State the preparation type.
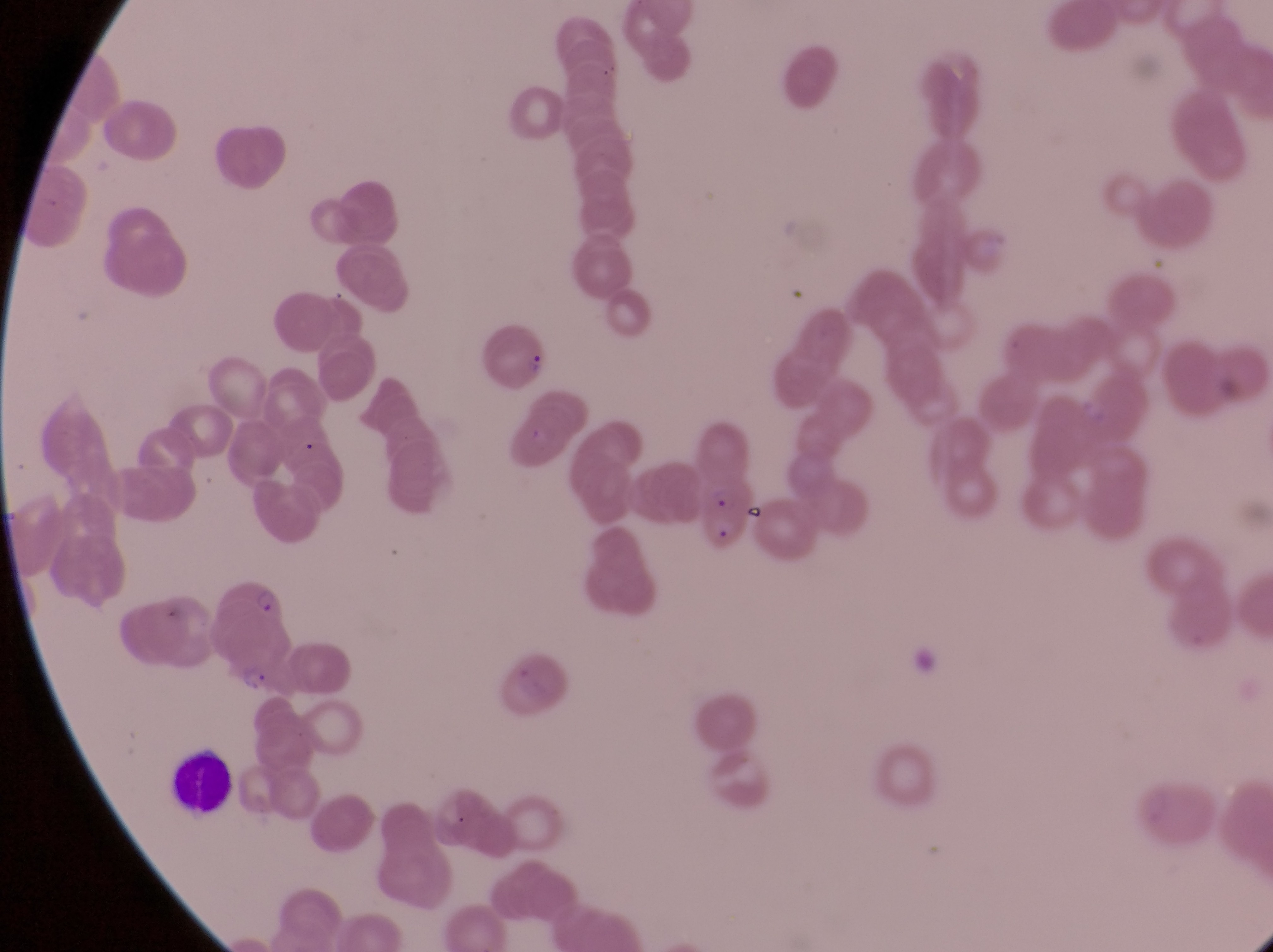

Thin blood smear.

Approximate bounding boxes as (left, top, right, bottom) in pixels.
Summary:
  - Leukocyte locations: (167, 754, 237, 816)
  - Parasitised red blood cell locations: (691, 475, 760, 552)
  - Trophozoite locations: (248, 580, 290, 619), (235, 661, 272, 698)
  - Country: Uganda
  - Image size: 1273×952 pixels
  - Magnification: 1000x
  - Capture: smartphone photograph through the eyepiece of an Olympus CX-23 microscope
  - Field of view: single